Report the malaria status of this cell.
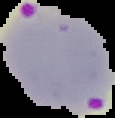
Parasitized.

From a thin blood smear. Image is 115×118 pixels. The area outside the segmented cell region is set to black.